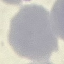

{
  "result": "no malaria parasites detected",
  "capture": "smartphone through the microscope eyepiece",
  "stain": "Giemsa",
  "preparation": "thin blood film",
  "image_type": "cell patch, automatically extracted from a larger field of view and resized to 64 × 64 pixels"
}